Locate every blood parasite and identify its species.
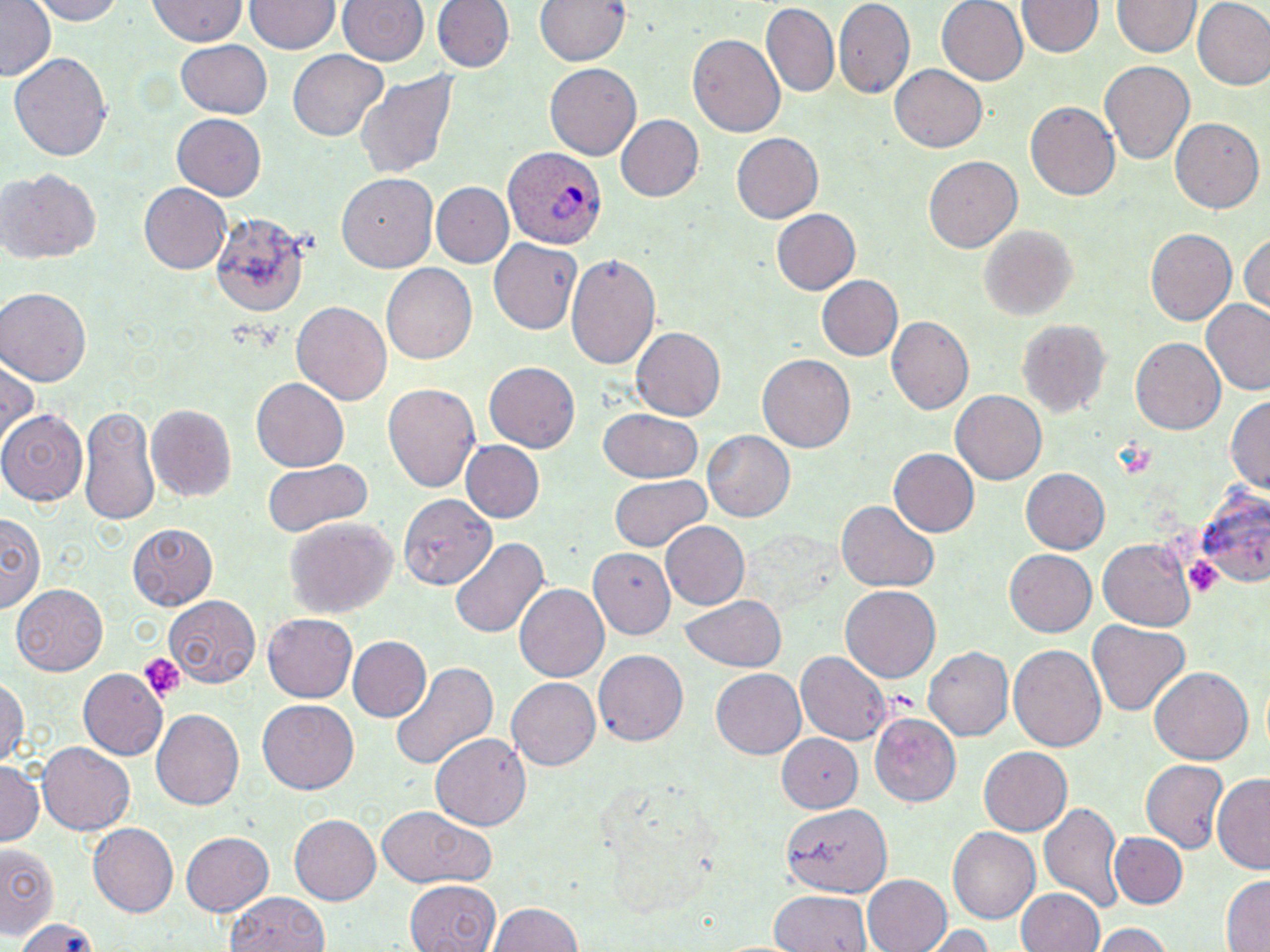

Approximate bounding boxes as (x1, y1, x2, y2) in pixels.
Plasmodium ovale-infected red blood cells: (503, 148, 604, 247).
No Plasmodium falciparum, Plasmodium malariae, Plasmodium vivax, Babesia divergens, or Trypanosoma brucei observed.

Platelet locations: (1182, 556, 1224, 598), (139, 652, 185, 701). Uninfected red blood cell locations: (0, 0, 55, 79), (32, 0, 123, 23), (335, 0, 429, 68), (431, 0, 511, 75), (535, 0, 628, 68), (834, 0, 918, 98), (936, 0, 1029, 85), (1193, 0, 1270, 89), (145, 1, 248, 46), (245, 1, 339, 56), (1020, 1, 1101, 58), (1115, 1, 1199, 58), (760, 6, 839, 98), (688, 32, 786, 138), (174, 41, 273, 119), (289, 51, 391, 141), (8, 53, 114, 163), (1100, 59, 1195, 163), (545, 61, 640, 158), (890, 66, 988, 152), (354, 69, 457, 183), (1025, 102, 1120, 202), (613, 113, 704, 201), (170, 114, 266, 201), (1168, 117, 1263, 215), (731, 132, 824, 225), (925, 156, 1022, 253), (1, 166, 102, 264), (338, 173, 437, 271), (137, 183, 232, 275), (430, 183, 512, 268), (771, 207, 861, 295), (206, 209, 310, 316), (980, 226, 1074, 319), (1146, 228, 1237, 327), (1239, 234, 1270, 316), (486, 237, 582, 334), (565, 252, 662, 375), (383, 262, 476, 367), (817, 274, 903, 360), (0, 287, 91, 386), (291, 298, 392, 405), (1200, 299, 1270, 395), (886, 317, 973, 414), (1016, 321, 1108, 417), (630, 327, 724, 421), (1131, 338, 1227, 436), (757, 353, 855, 455), (0, 357, 39, 454), (484, 362, 580, 453), (251, 380, 348, 469), (385, 383, 478, 495), (951, 390, 1049, 485), (1227, 392, 1270, 496), (79, 403, 162, 530), (147, 404, 237, 503), (599, 407, 705, 484), (0, 412, 86, 506), (704, 431, 796, 523), (460, 440, 544, 523), (889, 449, 977, 535), (261, 459, 372, 536), (1021, 467, 1110, 555), (610, 476, 711, 553), (1195, 488, 1270, 586), (401, 494, 498, 589), (835, 501, 939, 593), (3, 513, 42, 614), (284, 515, 398, 621), (659, 520, 750, 609), (126, 522, 216, 609), (449, 533, 548, 637), (1098, 539, 1193, 628), (591, 546, 675, 638), (1004, 549, 1097, 638), (515, 583, 609, 683), (840, 584, 940, 683), (11, 585, 108, 675), (679, 595, 787, 673), (167, 597, 261, 687), (263, 613, 357, 701), (1088, 619, 1190, 717), (346, 636, 431, 722), (1008, 643, 1107, 754), (923, 646, 1013, 740), (593, 650, 688, 746), (795, 652, 891, 744), (388, 662, 498, 775), (1148, 664, 1252, 763), (78, 669, 166, 761), (711, 670, 806, 756), (0, 677, 26, 773), (507, 677, 601, 771), (258, 698, 359, 791), (152, 709, 244, 811), (870, 712, 959, 807), (773, 732, 867, 818), (431, 733, 529, 831), (37, 743, 134, 835), (977, 747, 1071, 835), (1140, 760, 1228, 852), (0, 762, 43, 845), (1212, 774, 1270, 871), (1041, 801, 1123, 915), (375, 803, 490, 889), (783, 804, 892, 897), (290, 814, 381, 904), (88, 823, 179, 917), (946, 827, 1039, 924), (181, 830, 275, 916), (1110, 832, 1188, 908), (1, 844, 59, 938), (1217, 874, 1270, 952), (861, 875, 952, 952), (406, 880, 500, 952), (1015, 888, 1104, 952), (770, 890, 872, 952), (231, 894, 331, 952), (486, 900, 585, 952), (12, 918, 104, 952), (1089, 922, 1175, 952), (929, 925, 996, 952). Slide-level diagnosis: Plasmodium ovale. 1000x magnification. May-Grünwald-Giemsa-stained preparation. Thin blood film. Single field of view. Image is 1270×952 pixels. Optical microscopy.